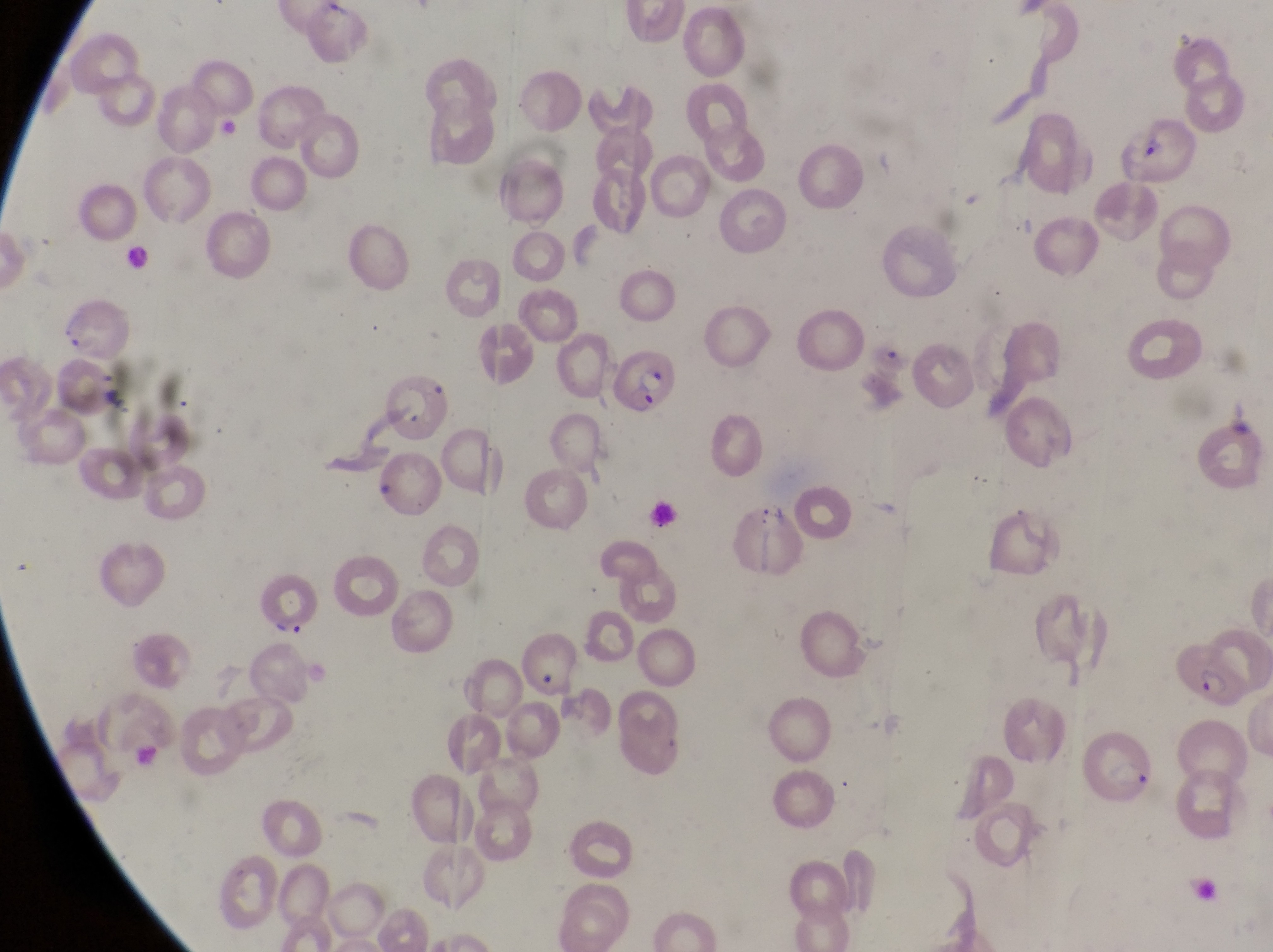 Approximate bounding boxes as [left, top, right, bottom] in pixels. Parasitised red blood cell locations: [1123, 117, 1201, 191], [58, 299, 131, 356], [604, 345, 679, 415], [382, 370, 444, 442], [731, 497, 805, 575], [1174, 642, 1248, 712], [1086, 729, 1158, 812]. Artifact (platelet-like body, stain precipitate, or debris) locations: [275, 619, 307, 639]. One field of view. Thin blood smear. Image is 1273×952 pixels. Captured by a smartphone held over the eyepiece of an Olympus CX-23 microscope. Collected in Uganda. Magnification of 1000x.